Identify the cell.
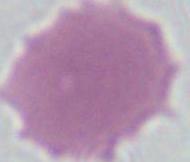

This is an erythrocyte.

Summary:
  - Magnification: 1000x
  - Modality: micrograph